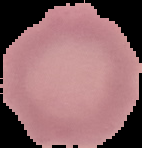
Summary:
  - Image type: segmented cell region with the area outside set to black
  - Malaria status: uninfected
  - Image size: 142×148 pixels
  - Preparation: thin blood film